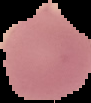

Result: no Plasmodium parasites seen. From a thin blood film. Image is 91×103 pixels. The area outside the segmented cell region is set to black.